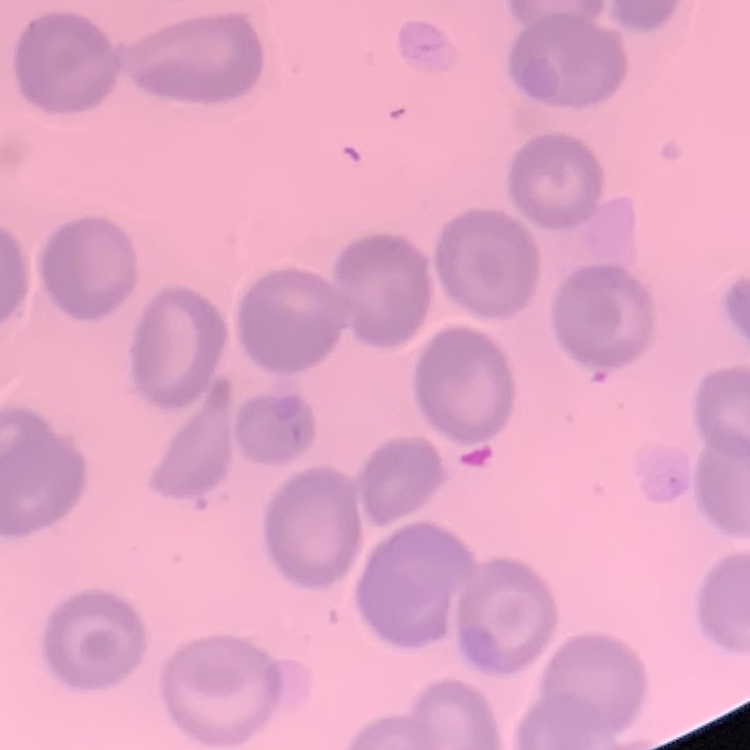

The red blood cells exhibit no rouleaux formation. One tile cut from a larger photomicrograph. Thin blood film. Stained with either Field's or Giemsa.